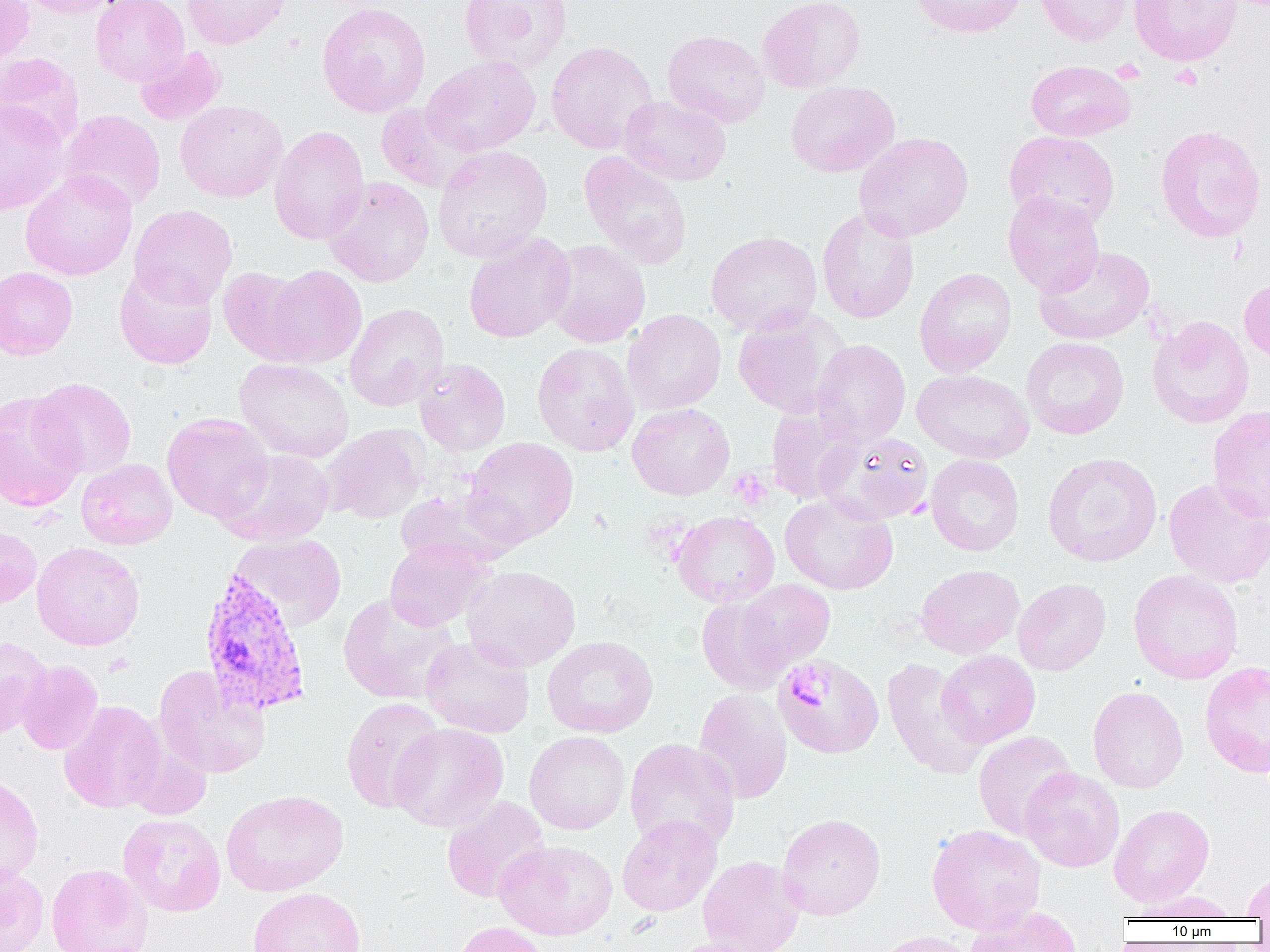
slide_level_diagnosis: Plasmodium vivax
modality: light microscopy
preparation: thin blood smear
image_size: 1270×952 pixels
field_of_view: one of a larger specimen
magnification: 1000x
platelet_locations: 'approximate bounding boxes as (x1,y1)-(x2,y2) corner pairs in pixels: (728,468)-(773,511), (786,666)-(834,713)'
plasmodium_vivax_infected_red_blood_cell_locations: 'approximate bounding boxes as (x1,y1)-(x2,y2) corner pairs in pixels: (197,568)-(313,717)'
uninfected_red_blood_cell_locations: 'approximate bounding boxes as (x1,y1)-(x2,y2) corner pairs in pixels: (0,0)-(35,70), (17,0)-(128,18), (90,0)-(189,86), (182,0)-(292,49), (458,0)-(572,74), (757,0)-(866,93), (911,0)-(1027,38), (1033,0)-(1134,46), (1129,0)-(1241,66), (317,1)-(431,118), (662,30)-(770,128), (546,41)-(659,154), (134,46)-(226,125), (0,52)-(85,147), (420,55)-(541,156), (1025,60)-(1136,141), (785,81)-(899,177), (620,95)-(731,186), (0,100)-(69,215), (175,100)-(288,203), (375,104)-(475,194), (59,109)-(166,213), (269,125)-(369,244), (1155,125)-(1266,243), (1004,131)-(1120,229), (854,132)-(974,241), (432,145)-(553,263), (578,151)-(693,269), (20,170)-(137,281), (323,176)-(435,287), (1003,192)-(1105,297), (129,205)-(237,308), (817,207)-(920,324), (706,231)-(822,336), (462,232)-(576,344), (544,240)-(650,347), (1033,246)-(1154,345), (114,265)-(218,369), (260,265)-(366,368), (0,266)-(78,360), (218,266)-(314,364), (914,267)-(1016,377), (1239,275)-(1270,367), (345,303)-(449,411), (732,308)-(850,418), (622,309)-(726,414), (1147,316)-(1254,428), (1021,336)-(1129,440), (812,339)-(911,445), (532,342)-(639,456), (234,357)-(354,462), (414,358)-(511,457), (912,369)-(1034,464), (31,378)-(136,478), (0,391)-(85,512), (765,401)-(865,504), (627,402)-(735,500), (1208,405)-(1270,521), (162,413)-(274,523), (322,425)-(429,524), (819,431)-(934,525), (463,437)-(579,546), (217,448)-(335,547), (1042,452)-(1162,567), (926,455)-(1024,556), (76,458)-(177,550), (1163,478)-(1270,589), (395,487)-(518,572), (780,494)-(898,595), (671,511)-(780,607), (0,528)-(41,608), (230,533)-(347,630), (384,539)-(491,631), (31,542)-(145,651), (915,564)-(1024,659), (462,565)-(581,672), (1128,569)-(1244,684), (1013,578)-(1111,675), (738,579)-(835,668), (337,592)-(461,705), (696,597)-(792,695), (542,635)-(659,738), (0,636)-(53,739), (421,636)-(535,738), (937,650)-(1040,747), (773,654)-(884,759), (882,658)-(987,780), (16,661)-(103,754), (1199,661)-(1270,778), (153,665)-(270,779), (1088,686)-(1187,793), (693,688)-(793,804), (341,696)-(444,814), (59,700)-(167,813), (389,723)-(509,832), (524,730)-(630,835), (973,730)-(1076,839), (122,732)-(213,819), (624,739)-(740,853), (1020,767)-(1125,872), (0,774)-(44,885), (221,789)-(349,896), (441,797)-(550,903), (1109,803)-(1214,907), (777,813)-(886,920), (117,814)-(226,917), (617,815)-(723,917), (926,823)-(1046,935), (494,839)-(618,941), (697,855)-(805,952), (0,861)-(48,952), (45,863)-(153,952), (1241,872)-(1270,919), (247,887)-(365,952), (1131,890)-(1239,921), (965,905)-(1081,952), (452,921)-(550,952), (876,931)-(983,952), (664,938)-(774,952)'